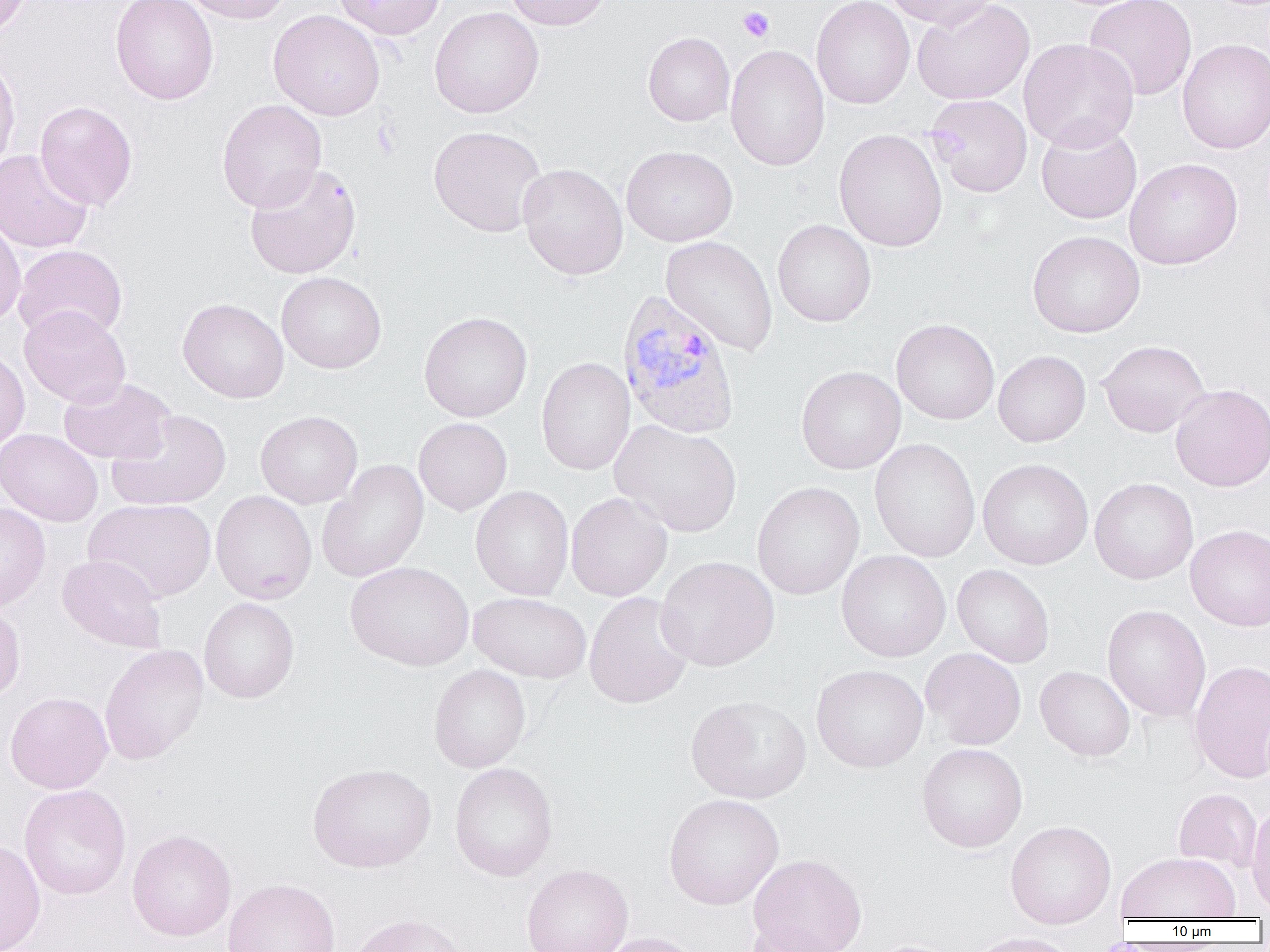
Approximate bounding boxes as named x1/y1/x2/y2 corners in pixels. Plasmodium vivax-infected red blood cell locations: (x1=616, y1=288, x2=741, y2=439). Platelet locations: (x1=738, y1=7, x2=774, y2=42). Uninfected red blood cell locations: (x1=0, y1=0, x2=32, y2=37), (x1=110, y1=0, x2=219, y2=105), (x1=180, y1=0, x2=293, y2=24), (x1=333, y1=0, x2=444, y2=40), (x1=505, y1=0, x2=614, y2=30), (x1=812, y1=0, x2=915, y2=109), (x1=884, y1=0, x2=998, y2=28), (x1=912, y1=0, x2=1034, y2=105), (x1=1083, y1=0, x2=1197, y2=100), (x1=430, y1=6, x2=544, y2=118), (x1=268, y1=9, x2=385, y2=120), (x1=643, y1=32, x2=735, y2=126), (x1=1019, y1=38, x2=1139, y2=151), (x1=1177, y1=38, x2=1270, y2=154), (x1=725, y1=44, x2=829, y2=171), (x1=0, y1=55, x2=20, y2=173), (x1=926, y1=94, x2=1033, y2=197), (x1=217, y1=99, x2=327, y2=212), (x1=35, y1=100, x2=137, y2=211), (x1=1036, y1=119, x2=1142, y2=225), (x1=429, y1=125, x2=547, y2=237), (x1=834, y1=129, x2=948, y2=251), (x1=621, y1=145, x2=737, y2=247), (x1=0, y1=149, x2=93, y2=253), (x1=1124, y1=158, x2=1243, y2=269), (x1=518, y1=163, x2=628, y2=280), (x1=245, y1=164, x2=361, y2=279), (x1=0, y1=216, x2=26, y2=327), (x1=773, y1=219, x2=876, y2=327), (x1=1027, y1=230, x2=1145, y2=338), (x1=661, y1=236, x2=778, y2=355), (x1=13, y1=245, x2=127, y2=342), (x1=276, y1=271, x2=386, y2=374), (x1=178, y1=298, x2=289, y2=403), (x1=19, y1=306, x2=130, y2=408), (x1=419, y1=311, x2=532, y2=421), (x1=891, y1=318, x2=999, y2=425), (x1=1097, y1=340, x2=1211, y2=437), (x1=0, y1=349, x2=29, y2=453), (x1=993, y1=350, x2=1090, y2=447), (x1=536, y1=358, x2=636, y2=475), (x1=796, y1=366, x2=906, y2=474), (x1=58, y1=378, x2=175, y2=465), (x1=1170, y1=384, x2=1270, y2=492), (x1=107, y1=410, x2=232, y2=511), (x1=256, y1=410, x2=362, y2=509), (x1=413, y1=418, x2=512, y2=515), (x1=610, y1=420, x2=742, y2=537), (x1=0, y1=428, x2=103, y2=526), (x1=869, y1=438, x2=981, y2=562), (x1=317, y1=459, x2=429, y2=583), (x1=977, y1=459, x2=1093, y2=569), (x1=1089, y1=477, x2=1199, y2=584), (x1=752, y1=482, x2=865, y2=600), (x1=471, y1=486, x2=574, y2=600), (x1=211, y1=490, x2=317, y2=604), (x1=565, y1=493, x2=672, y2=601), (x1=84, y1=498, x2=216, y2=602), (x1=0, y1=502, x2=51, y2=612), (x1=1185, y1=524, x2=1270, y2=631), (x1=836, y1=550, x2=951, y2=662), (x1=57, y1=554, x2=168, y2=654), (x1=656, y1=556, x2=779, y2=671), (x1=345, y1=561, x2=474, y2=671), (x1=952, y1=564, x2=1055, y2=668), (x1=584, y1=591, x2=694, y2=709), (x1=469, y1=592, x2=591, y2=683), (x1=198, y1=597, x2=299, y2=703), (x1=0, y1=603, x2=25, y2=703), (x1=1102, y1=605, x2=1210, y2=721), (x1=99, y1=643, x2=209, y2=764), (x1=920, y1=648, x2=1026, y2=750), (x1=1189, y1=660, x2=1270, y2=783), (x1=429, y1=664, x2=531, y2=773), (x1=811, y1=664, x2=929, y2=772), (x1=1035, y1=666, x2=1135, y2=761), (x1=5, y1=691, x2=114, y2=794), (x1=686, y1=695, x2=812, y2=803), (x1=917, y1=743, x2=1028, y2=852), (x1=449, y1=762, x2=558, y2=881), (x1=307, y1=763, x2=436, y2=873), (x1=19, y1=784, x2=131, y2=900), (x1=1173, y1=788, x2=1263, y2=872), (x1=663, y1=793, x2=784, y2=910), (x1=1246, y1=802, x2=1270, y2=917), (x1=1004, y1=820, x2=1116, y2=929), (x1=127, y1=829, x2=236, y2=941), (x1=0, y1=839, x2=45, y2=952), (x1=1116, y1=852, x2=1240, y2=922), (x1=748, y1=854, x2=867, y2=952), (x1=521, y1=863, x2=633, y2=952), (x1=223, y1=879, x2=341, y2=952), (x1=347, y1=912, x2=476, y2=952), (x1=741, y1=921, x2=848, y2=952), (x1=597, y1=931, x2=703, y2=952), (x1=967, y1=932, x2=1080, y2=952), (x1=866, y1=940, x2=963, y2=952). Slide-level diagnosis: Plasmodium vivax. Light microscopy. Captured at 1000x magnification. Image is 1270×952 pixels. One field of a larger specimen. Thin blood smear.